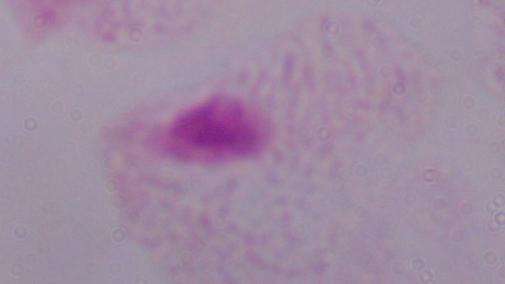

A trichomonad is shown. 1000x magnification. Micrograph.